Outline each blood parasite and name the species.
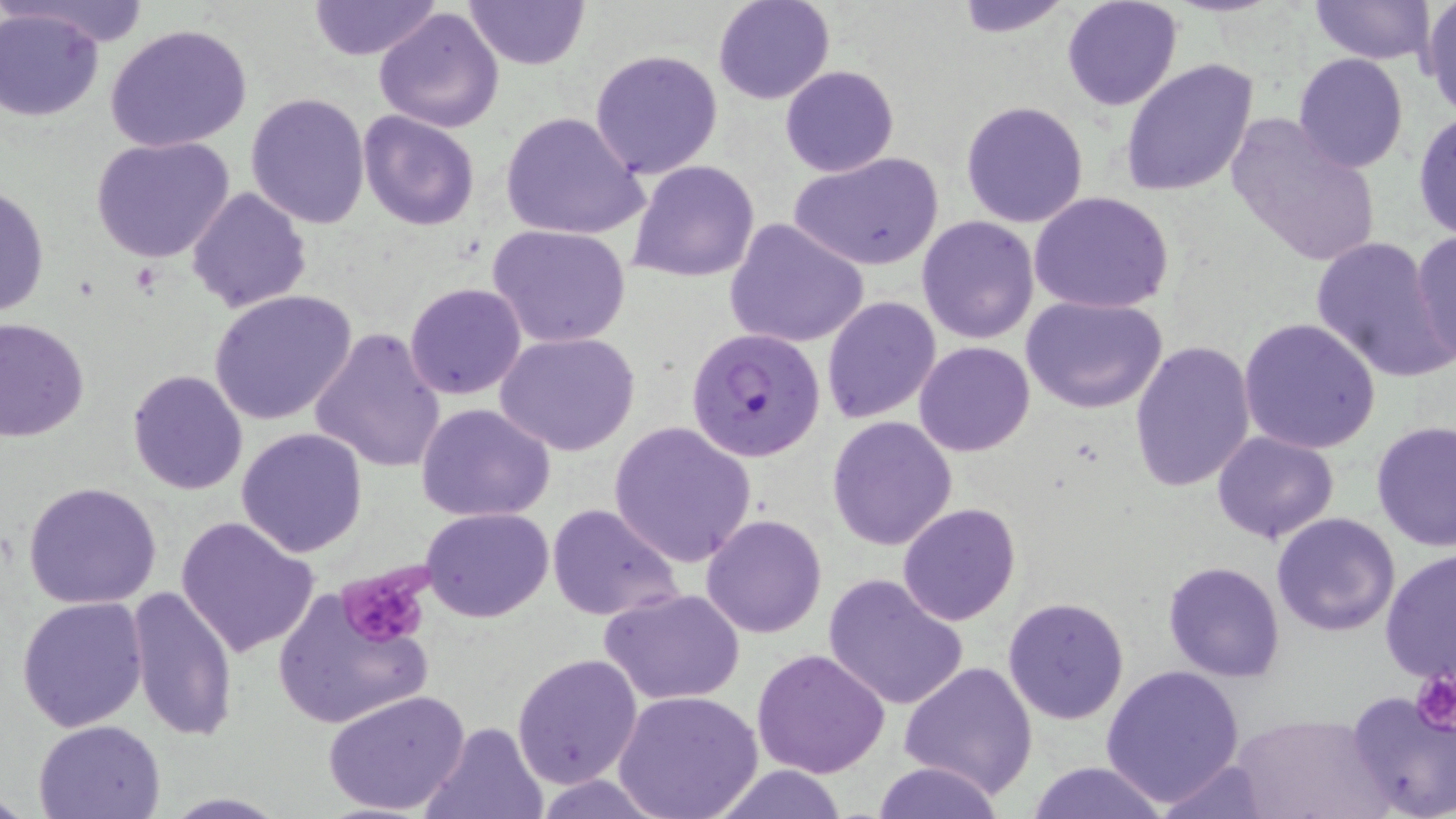

Approximate bounding boxes as [x1, y1, x2, y2] in pixels.
Plasmodium falciparum-infected red blood cells: [687, 326, 826, 461].
No Plasmodium ovale, Plasmodium malariae, Plasmodium vivax, Babesia divergens, or Trypanosoma brucei observed.

Uninfected red blood cell locations: [17, 0, 153, 48], [306, 0, 443, 62], [463, 0, 588, 70], [713, 0, 834, 104], [950, 0, 1074, 35], [1061, 0, 1183, 111], [1308, 0, 1437, 66], [1422, 2, 1455, 116], [373, 5, 505, 133], [0, 8, 106, 122], [105, 22, 256, 155], [588, 47, 723, 179], [1293, 53, 1409, 173], [1121, 59, 1257, 198], [780, 65, 899, 177], [245, 92, 372, 229], [960, 100, 1091, 228], [358, 110, 480, 232], [1225, 110, 1383, 269], [499, 111, 647, 243], [1412, 111, 1456, 241], [92, 134, 236, 264], [789, 151, 944, 271], [629, 160, 761, 284], [1, 184, 49, 321], [187, 187, 311, 314], [1029, 192, 1174, 314], [917, 214, 1040, 343], [725, 220, 870, 350], [487, 224, 632, 348], [1409, 229, 1456, 369], [1310, 235, 1448, 380], [405, 282, 528, 401], [208, 291, 358, 427], [1019, 294, 1168, 413], [821, 296, 941, 424], [1239, 316, 1382, 453], [1, 317, 90, 441], [309, 326, 445, 472], [497, 332, 640, 456], [1129, 340, 1256, 493], [914, 341, 1035, 456], [127, 370, 248, 495], [416, 402, 554, 521], [827, 416, 957, 550], [607, 420, 757, 567], [1372, 421, 1456, 554], [236, 427, 368, 557], [1212, 431, 1340, 544], [24, 482, 164, 608], [898, 502, 1020, 625], [547, 503, 684, 623], [421, 506, 554, 622], [1271, 512, 1401, 638], [173, 514, 321, 658], [701, 514, 827, 638], [1380, 549, 1456, 685], [1162, 560, 1286, 681], [823, 573, 970, 711], [271, 582, 435, 732], [124, 586, 238, 742], [600, 587, 746, 706], [16, 594, 150, 733], [1002, 596, 1130, 724], [751, 647, 890, 779], [512, 653, 643, 790], [899, 660, 1039, 797], [1100, 664, 1247, 805], [1343, 687, 1455, 819], [323, 688, 470, 817], [614, 691, 763, 819], [1230, 713, 1384, 819], [34, 718, 168, 818], [422, 720, 547, 819], [1151, 758, 1275, 817], [867, 760, 1008, 818], [1024, 761, 1172, 817], [705, 764, 853, 818], [532, 775, 673, 817], [160, 793, 289, 817]. Platelet locations: [333, 564, 434, 651], [1410, 667, 1456, 737]. Slide-level diagnosis: Plasmodium falciparum. Single field of view. Thin blood smear. May-Grünwald-Giemsa stain. Light microscopy. Captured at 1000x magnification. Image is 1456×819 pixels.